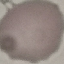

Malaria status: uninfected. Photographed with a smartphone camera at the microscope eyepiece. Cell patch, automatically extracted from a larger field of view and resized to 64 × 64 pixels. Thin blood film. Giemsa-stained preparation.